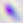

magnification = 400x
modality = photomicrograph
identification = Toxoplasma gondii